Classify this cell by malaria status.
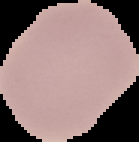
It is uninfected.

preparation: thin blood smear
image_type: cell region segmented out of the field of view; surrounding area masked to black
image_size: 139×142 pixels